Classify this cell by malaria status.
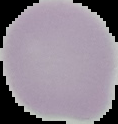
It is uninfected.

From a thin blood film. Image is 118×124 pixels. Segmented cell region on a black background.